Classify this cell by malaria status.
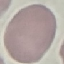

It is uninfected.

image_type: automatically extracted cell patch, resized to 64 × 64 pixels
stain: Giemsa
capture: smartphone camera at the microscope eyepiece
preparation: thin blood film